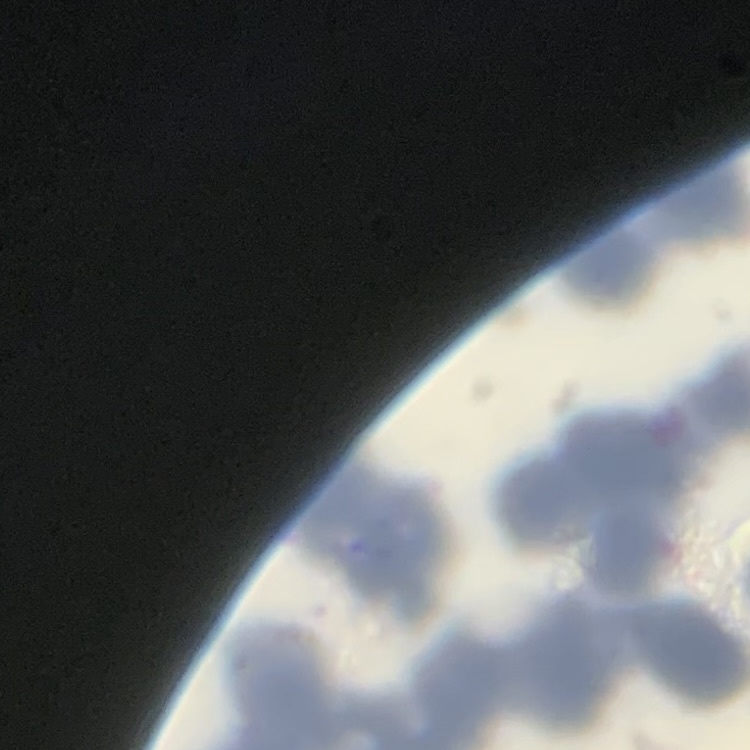
Summary:
  - Erythrocyte morphology: rouleaux formation
  - Image type: square crop of a larger photomicrograph
  - Preparation: thin peripheral smear
  - Stain: Field's or Giemsa